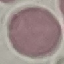

{
  "result": "no malaria parasites seen",
  "preparation": "thin blood film",
  "image_type": "cell patch, automatically extracted from a larger field of view and resized to 64 × 64 pixels",
  "capture": "smartphone through the microscope eyepiece",
  "stain": "Giemsa"
}